Locate and identify every blood parasite.
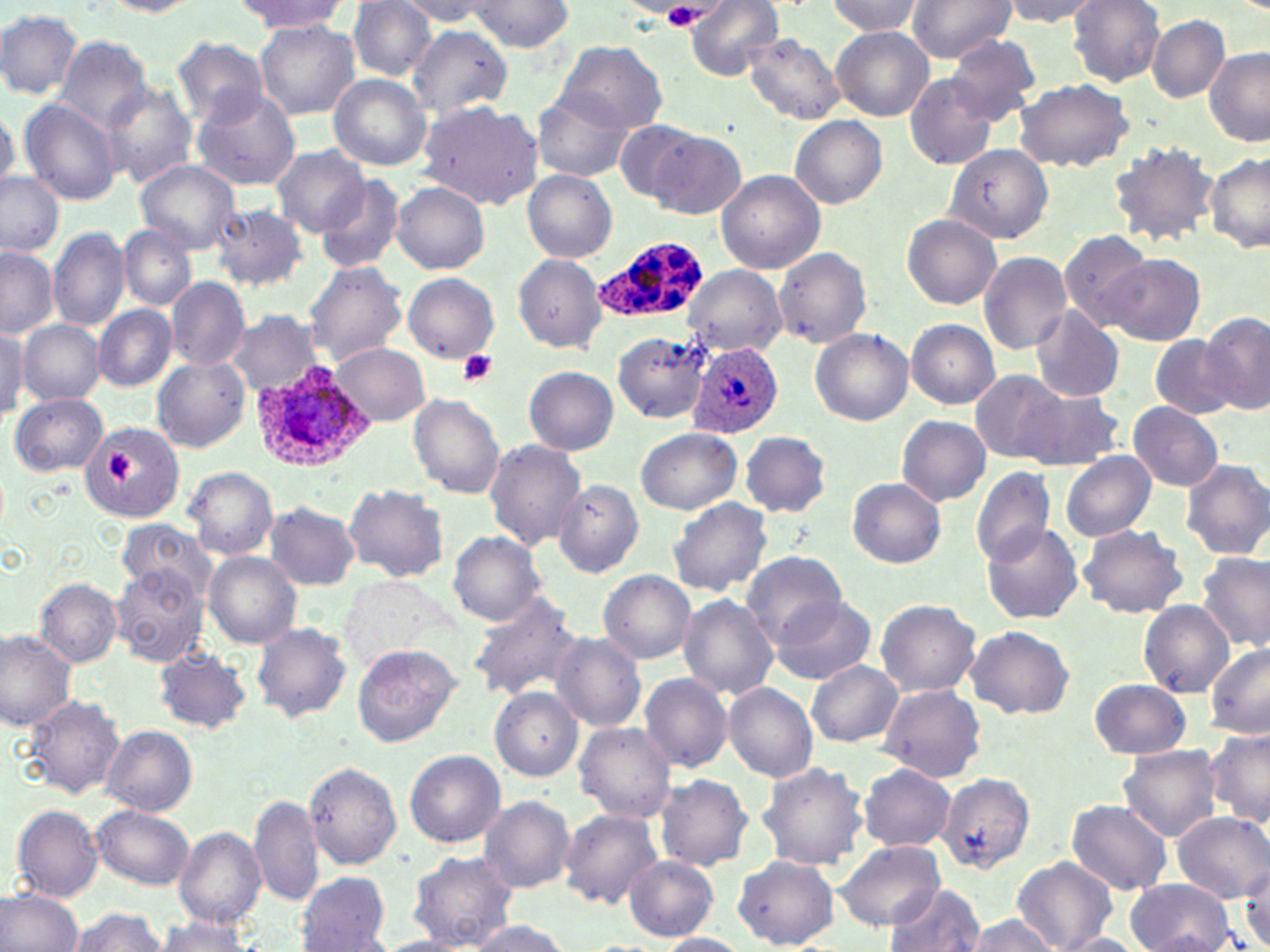

Approximate bounding boxes as named x1/y1/x2/y2 corners in pixels.
Plasmodium ovale-infected red blood cells: (x1=591, y1=234, x2=707, y2=325), (x1=687, y1=341, x2=784, y2=439), (x1=249, y1=360, x2=373, y2=476).
No Plasmodium falciparum, Plasmodium malariae, Plasmodium vivax, Babesia divergens, or Trypanosoma brucei observed.

Platelet locations: (x1=661, y1=5, x2=702, y2=32), (x1=457, y1=351, x2=498, y2=387), (x1=105, y1=452, x2=132, y2=483). Uninfected red blood cell locations: (x1=103, y1=0, x2=202, y2=16), (x1=906, y1=0, x2=1016, y2=63), (x1=998, y1=0, x2=1102, y2=25), (x1=232, y1=1, x2=349, y2=33), (x1=346, y1=1, x2=437, y2=79), (x1=401, y1=1, x2=493, y2=28), (x1=465, y1=1, x2=574, y2=52), (x1=684, y1=1, x2=785, y2=80), (x1=824, y1=1, x2=924, y2=37), (x1=1067, y1=1, x2=1166, y2=86), (x1=0, y1=9, x2=83, y2=99), (x1=1146, y1=15, x2=1229, y2=103), (x1=255, y1=21, x2=360, y2=120), (x1=407, y1=25, x2=513, y2=120), (x1=831, y1=27, x2=934, y2=120), (x1=57, y1=35, x2=152, y2=133), (x1=744, y1=35, x2=845, y2=124), (x1=945, y1=35, x2=1043, y2=123), (x1=173, y1=37, x2=270, y2=128), (x1=555, y1=40, x2=667, y2=135), (x1=1204, y1=46, x2=1270, y2=148), (x1=328, y1=73, x2=431, y2=169), (x1=903, y1=74, x2=999, y2=171), (x1=1011, y1=78, x2=1134, y2=171), (x1=101, y1=84, x2=197, y2=188), (x1=191, y1=89, x2=303, y2=191), (x1=531, y1=90, x2=636, y2=183), (x1=19, y1=99, x2=121, y2=206), (x1=416, y1=101, x2=542, y2=208), (x1=0, y1=112, x2=19, y2=192), (x1=789, y1=115, x2=886, y2=209), (x1=613, y1=119, x2=708, y2=204), (x1=642, y1=129, x2=745, y2=220), (x1=1108, y1=140, x2=1220, y2=245), (x1=272, y1=144, x2=370, y2=237), (x1=945, y1=145, x2=1052, y2=244), (x1=1205, y1=152, x2=1270, y2=251), (x1=134, y1=159, x2=244, y2=252), (x1=715, y1=169, x2=826, y2=275), (x1=522, y1=170, x2=615, y2=262), (x1=0, y1=172, x2=64, y2=257), (x1=316, y1=174, x2=406, y2=274), (x1=392, y1=182, x2=489, y2=274), (x1=212, y1=204, x2=307, y2=292), (x1=902, y1=214, x2=1001, y2=310), (x1=119, y1=224, x2=196, y2=311), (x1=47, y1=227, x2=129, y2=333), (x1=1058, y1=229, x2=1151, y2=327), (x1=772, y1=247, x2=871, y2=347), (x1=0, y1=249, x2=58, y2=337), (x1=977, y1=251, x2=1072, y2=356), (x1=513, y1=253, x2=608, y2=353), (x1=1098, y1=254, x2=1206, y2=345), (x1=304, y1=261, x2=408, y2=365), (x1=403, y1=272, x2=498, y2=361), (x1=166, y1=276, x2=250, y2=371), (x1=93, y1=305, x2=177, y2=391), (x1=1030, y1=308, x2=1124, y2=402), (x1=1200, y1=311, x2=1270, y2=415), (x1=225, y1=312, x2=326, y2=393), (x1=19, y1=319, x2=105, y2=404), (x1=906, y1=320, x2=999, y2=408), (x1=0, y1=326, x2=28, y2=415), (x1=809, y1=327, x2=913, y2=425), (x1=614, y1=331, x2=710, y2=423), (x1=1150, y1=335, x2=1239, y2=419), (x1=331, y1=344, x2=431, y2=425), (x1=152, y1=357, x2=251, y2=452), (x1=523, y1=366, x2=619, y2=455), (x1=971, y1=370, x2=1069, y2=462), (x1=1017, y1=383, x2=1126, y2=470), (x1=407, y1=393, x2=505, y2=499), (x1=12, y1=394, x2=108, y2=476), (x1=1127, y1=402, x2=1224, y2=492), (x1=897, y1=415, x2=989, y2=505), (x1=80, y1=419, x2=187, y2=524), (x1=637, y1=428, x2=740, y2=515), (x1=740, y1=431, x2=830, y2=519), (x1=484, y1=439, x2=586, y2=550), (x1=1061, y1=450, x2=1155, y2=542), (x1=1180, y1=458, x2=1270, y2=560), (x1=972, y1=466, x2=1057, y2=567), (x1=186, y1=467, x2=278, y2=559), (x1=847, y1=477, x2=948, y2=567), (x1=553, y1=479, x2=643, y2=578), (x1=343, y1=483, x2=448, y2=583), (x1=667, y1=497, x2=772, y2=597), (x1=265, y1=502, x2=359, y2=590), (x1=119, y1=519, x2=213, y2=599), (x1=982, y1=521, x2=1084, y2=625), (x1=1076, y1=524, x2=1189, y2=619), (x1=449, y1=531, x2=547, y2=625), (x1=203, y1=550, x2=302, y2=648), (x1=740, y1=550, x2=845, y2=647), (x1=1197, y1=552, x2=1268, y2=651), (x1=109, y1=565, x2=209, y2=667), (x1=598, y1=569, x2=697, y2=663), (x1=34, y1=578, x2=122, y2=667), (x1=343, y1=579, x2=444, y2=667), (x1=466, y1=593, x2=582, y2=702), (x1=677, y1=594, x2=779, y2=699), (x1=770, y1=595, x2=878, y2=685), (x1=875, y1=599, x2=981, y2=696), (x1=1138, y1=599, x2=1233, y2=697), (x1=252, y1=623, x2=352, y2=723), (x1=965, y1=626, x2=1074, y2=719), (x1=0, y1=631, x2=77, y2=731), (x1=550, y1=633, x2=646, y2=733), (x1=1205, y1=644, x2=1270, y2=738), (x1=352, y1=645, x2=461, y2=748), (x1=153, y1=649, x2=250, y2=732), (x1=806, y1=660, x2=904, y2=747), (x1=639, y1=672, x2=735, y2=773), (x1=1090, y1=678, x2=1190, y2=759), (x1=723, y1=682, x2=816, y2=784), (x1=876, y1=683, x2=987, y2=782), (x1=490, y1=687, x2=583, y2=781), (x1=864, y1=693, x2=974, y2=848), (x1=25, y1=694, x2=127, y2=799), (x1=574, y1=722, x2=677, y2=822), (x1=103, y1=725, x2=198, y2=816), (x1=1205, y1=727, x2=1270, y2=831), (x1=1117, y1=746, x2=1222, y2=840), (x1=403, y1=750, x2=506, y2=848), (x1=755, y1=760, x2=869, y2=872), (x1=305, y1=762, x2=403, y2=870), (x1=860, y1=764, x2=956, y2=850), (x1=653, y1=774, x2=753, y2=872), (x1=936, y1=774, x2=1035, y2=877), (x1=249, y1=793, x2=323, y2=910), (x1=480, y1=795, x2=576, y2=892), (x1=1067, y1=799, x2=1174, y2=895), (x1=9, y1=804, x2=104, y2=903), (x1=93, y1=805, x2=196, y2=889), (x1=559, y1=808, x2=664, y2=911), (x1=1173, y1=813, x2=1268, y2=901), (x1=173, y1=826, x2=265, y2=930), (x1=833, y1=839, x2=944, y2=932), (x1=408, y1=852, x2=519, y2=949), (x1=623, y1=856, x2=718, y2=939), (x1=734, y1=856, x2=839, y2=948), (x1=1011, y1=859, x2=1116, y2=950), (x1=296, y1=872, x2=391, y2=950), (x1=1126, y1=878, x2=1239, y2=952), (x1=884, y1=884, x2=984, y2=952), (x1=1, y1=888, x2=84, y2=952), (x1=64, y1=907, x2=169, y2=951), (x1=961, y1=914, x2=1058, y2=951), (x1=153, y1=916, x2=254, y2=951), (x1=461, y1=919, x2=572, y2=951), (x1=653, y1=933, x2=752, y2=952), (x1=1054, y1=933, x2=1145, y2=952), (x1=375, y1=935, x2=482, y2=952). Slide-level diagnosis: Plasmodium ovale. 1000x magnification. Thin blood smear. Single field of view. Light microscopy. Image is 1270×952 pixels. May-Grünwald-Giemsa-stained preparation.